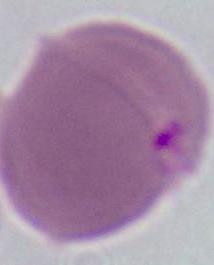
identification: red blood cell
modality: micrograph
magnification: 1000x